Report the malaria status of this cell.
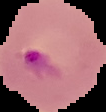
Parasitized.

image_size: 106×112 pixels
image_type: segmented cell region on a black background
preparation: thin blood smear